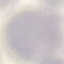
result = no malaria parasites seen
stain = Giemsa
capture = smartphone camera at the microscope eyepiece
preparation = thin smear
image type = cell patch, automatically extracted from a larger field of view and resized to 64 × 64 pixels